Give the extent of all uninfected red blood cells.
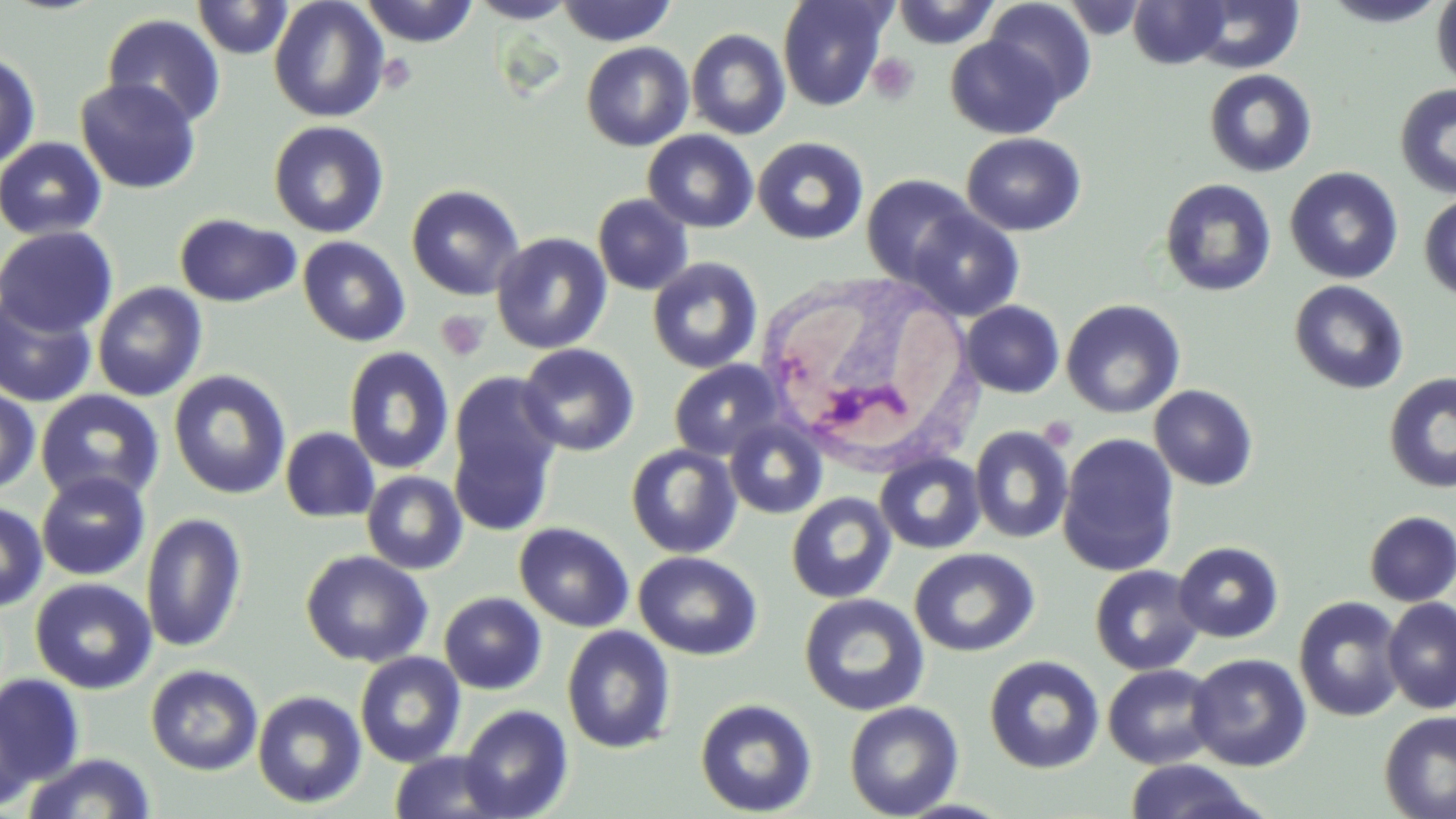
Approximate bounding boxes as [x1, y1, x2, y2] in pixels.
Uninfected red blood cells: [192, 0, 294, 60], [268, 0, 390, 123], [359, 0, 479, 47], [468, 0, 577, 23], [777, 0, 892, 112], [889, 0, 1001, 48], [1058, 0, 1150, 40], [1320, 0, 1451, 27], [1431, 0, 1456, 90], [555, 1, 677, 46], [984, 1, 1096, 106], [1128, 1, 1231, 69], [1185, 1, 1305, 73], [101, 13, 226, 128], [686, 28, 791, 140], [945, 34, 1066, 140], [581, 42, 694, 151], [0, 51, 42, 171], [1203, 69, 1317, 178], [75, 77, 201, 194], [1395, 82, 1455, 200], [268, 120, 390, 238], [642, 129, 759, 233], [961, 132, 1086, 236], [753, 136, 869, 245], [0, 137, 108, 241], [1284, 167, 1404, 284], [861, 174, 979, 286], [1159, 178, 1277, 297], [406, 184, 525, 301], [592, 194, 694, 295], [1419, 194, 1456, 301], [906, 209, 1025, 321], [174, 213, 301, 308], [0, 225, 119, 337], [491, 233, 612, 354], [297, 236, 411, 347], [647, 257, 763, 374], [1289, 280, 1409, 394], [92, 282, 208, 401], [0, 294, 98, 408], [1061, 298, 1186, 418], [960, 300, 1064, 398], [517, 343, 640, 456], [343, 347, 455, 474], [669, 360, 783, 461], [168, 370, 292, 500], [448, 370, 564, 534], [1383, 372, 1456, 493], [1149, 384, 1258, 491], [0, 385, 41, 494], [34, 389, 165, 506], [724, 419, 828, 519], [969, 425, 1074, 544], [280, 426, 380, 523], [1057, 432, 1180, 577], [625, 443, 742, 559], [874, 452, 986, 554], [361, 470, 468, 575], [36, 471, 151, 581], [786, 492, 897, 604], [0, 501, 48, 613], [1363, 510, 1456, 606], [141, 512, 248, 654], [514, 522, 634, 632], [1173, 541, 1284, 643], [909, 547, 1040, 657], [300, 550, 433, 668], [633, 550, 762, 660], [1089, 564, 1205, 676], [30, 577, 157, 695], [439, 591, 547, 695], [799, 593, 929, 716], [1293, 596, 1406, 722], [1381, 596, 1456, 714], [561, 626, 676, 754], [354, 652, 466, 768], [1187, 653, 1312, 772], [984, 655, 1105, 774], [145, 664, 263, 775], [1102, 664, 1222, 769], [0, 674, 84, 787], [252, 690, 367, 808], [694, 697, 818, 817], [844, 700, 965, 818], [459, 704, 574, 818], [0, 706, 36, 811], [1378, 710, 1456, 819], [388, 750, 512, 819], [22, 752, 156, 819], [1122, 759, 1267, 818].

slide-level diagnosis = no evidence of blood parasites
preparation = thin blood smear
modality = light microscopy
image size = 1456×819 pixels
stain = May-Grünwald-Giemsa
field of view = one of a larger specimen
platelet locations = approximate bounding boxes as [x1, y1, x2, y2] in pixels: [867, 53, 920, 105], [436, 310, 490, 362], [1038, 416, 1078, 451]
magnification = 1000x
white blood cell locations = approximate bounding boxes as [x1, y1, x2, y2] in pixels: [756, 271, 979, 469]